Outline every Plasmodium parasite, every leukocyte, and every artifact (stain precipitate or debris).
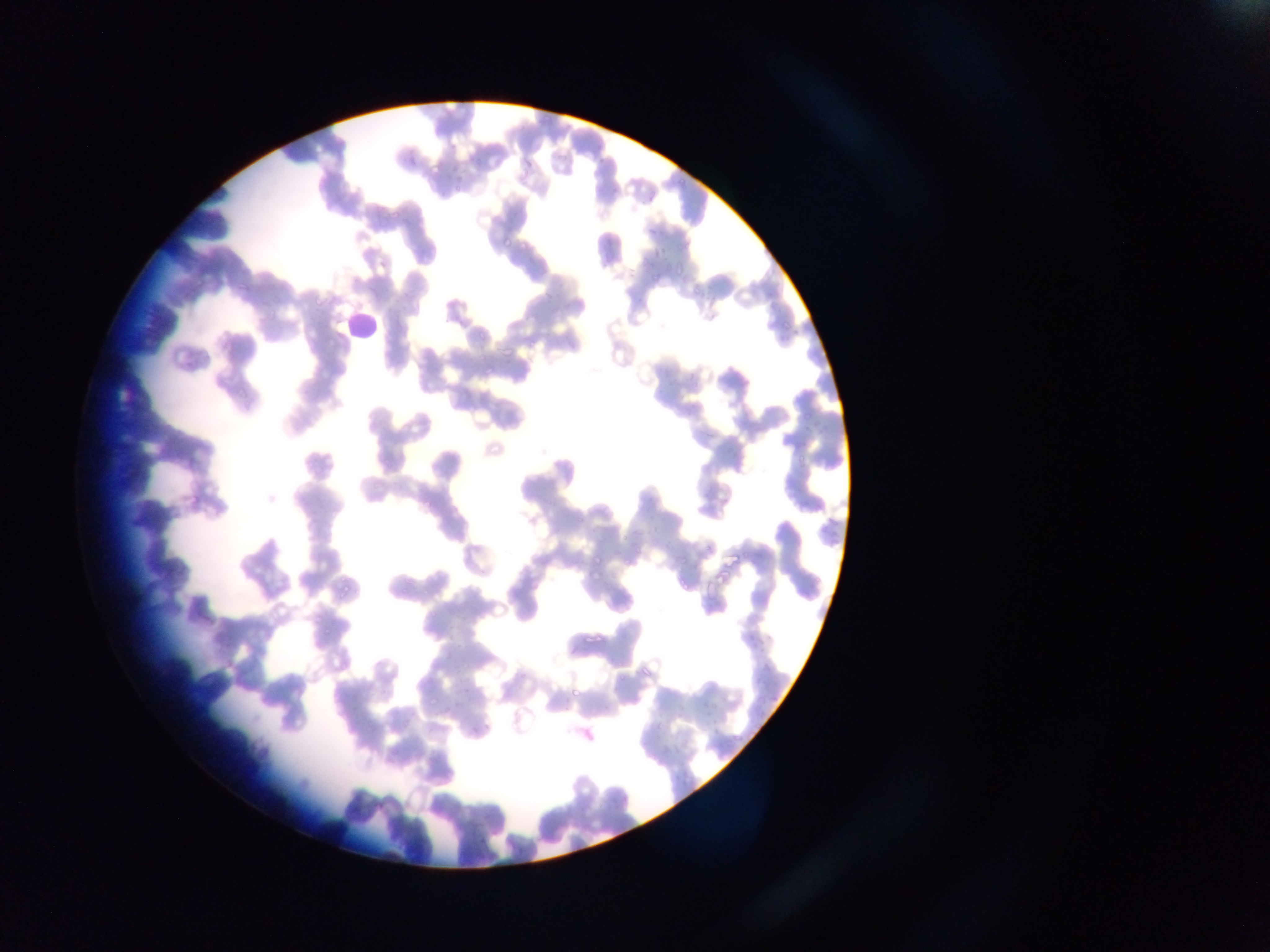
Approximate bounding boxes as [left, top, right, bottom] in pixels.
Plasmodium parasites: [646, 226, 660, 236], [500, 230, 518, 249], [517, 237, 531, 251], [649, 245, 670, 260], [670, 264, 684, 277], [780, 319, 795, 329], [526, 337, 536, 351], [503, 348, 514, 358], [484, 363, 494, 378], [590, 549, 604, 565], [715, 568, 732, 582], [590, 572, 604, 584], [339, 581, 353, 601], [580, 627, 610, 643], [569, 686, 583, 696], [426, 696, 440, 706].
Leukocytes: [341, 311, 384, 342].

capture = mobile-phone photograph through a microscope
field of view = single
image size = 1270×952 pixels
preparation = thin blood smear
country = Ghana